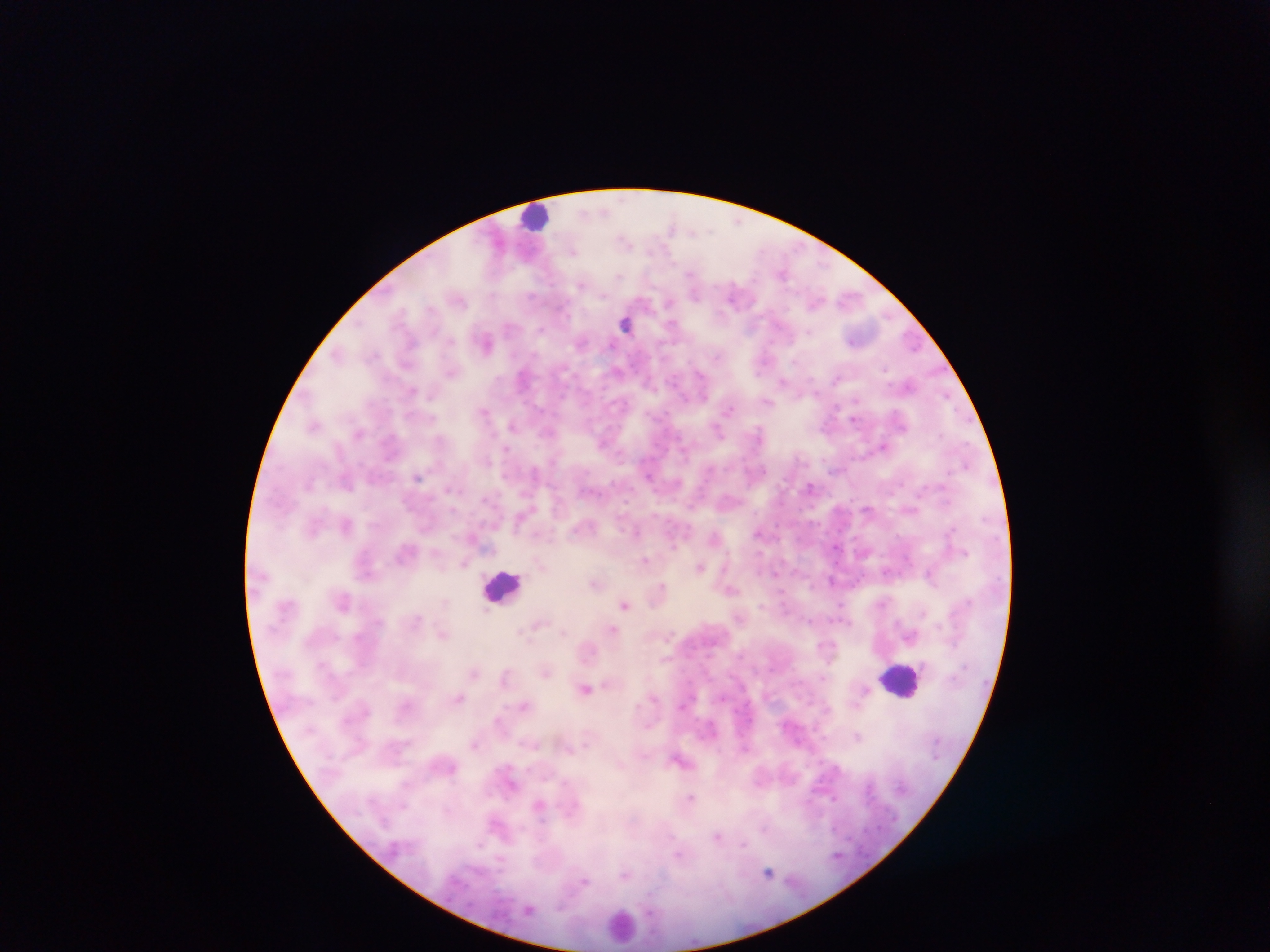 Approximate centers as x y in pixels. Leukocyte locations: 536 216; 503 585; 903 680; 621 924. Plasmodium parasite locations: 603 211; 671 226; 624 241; 572 251; 690 274; 619 276; 581 285; 694 294; 531 295; 732 295; 460 300; 668 303; 430 309; 626 324; 671 326; 509 327; 541 329; 809 332; 581 342; 411 343; 486 343; 336 354; 715 355; 885 369; 452 373; 700 374; 523 377; 782 382; 412 391; 814 392; 946 395; 704 396; 856 401; 768 402; 728 410; 484 412; 854 419; 314 425; 512 425; 718 431; 758 432; 883 446; 507 450; 966 465; 419 477; 649 477; 346 483; 810 486; 869 510; 346 525; 952 529; 636 532; 758 533; 715 537; 673 544; 405 552; 965 552; 645 560; 465 563; 700 567; 886 571; 775 573; 929 574; 832 581; 594 583; 661 585; 731 590; 444 601; 625 604; 841 606; 487 610; 417 619; 539 623; 612 629; 520 631; 562 632; 443 635; 474 671; 546 671; 505 675; 823 678; 585 688; 459 698; 524 705; 498 719; 857 736; 474 745; 569 748; 678 761; 691 797; 539 804; 764 828; 718 836; 744 844; 678 854; 500 859; 768 872; 625 874; 585 881; 529 910. Image is 1270×952 pixels. Single field of view. Collected in Ghana. Photographed through a microscope with a mobile-phone camera. Thick blood smear.